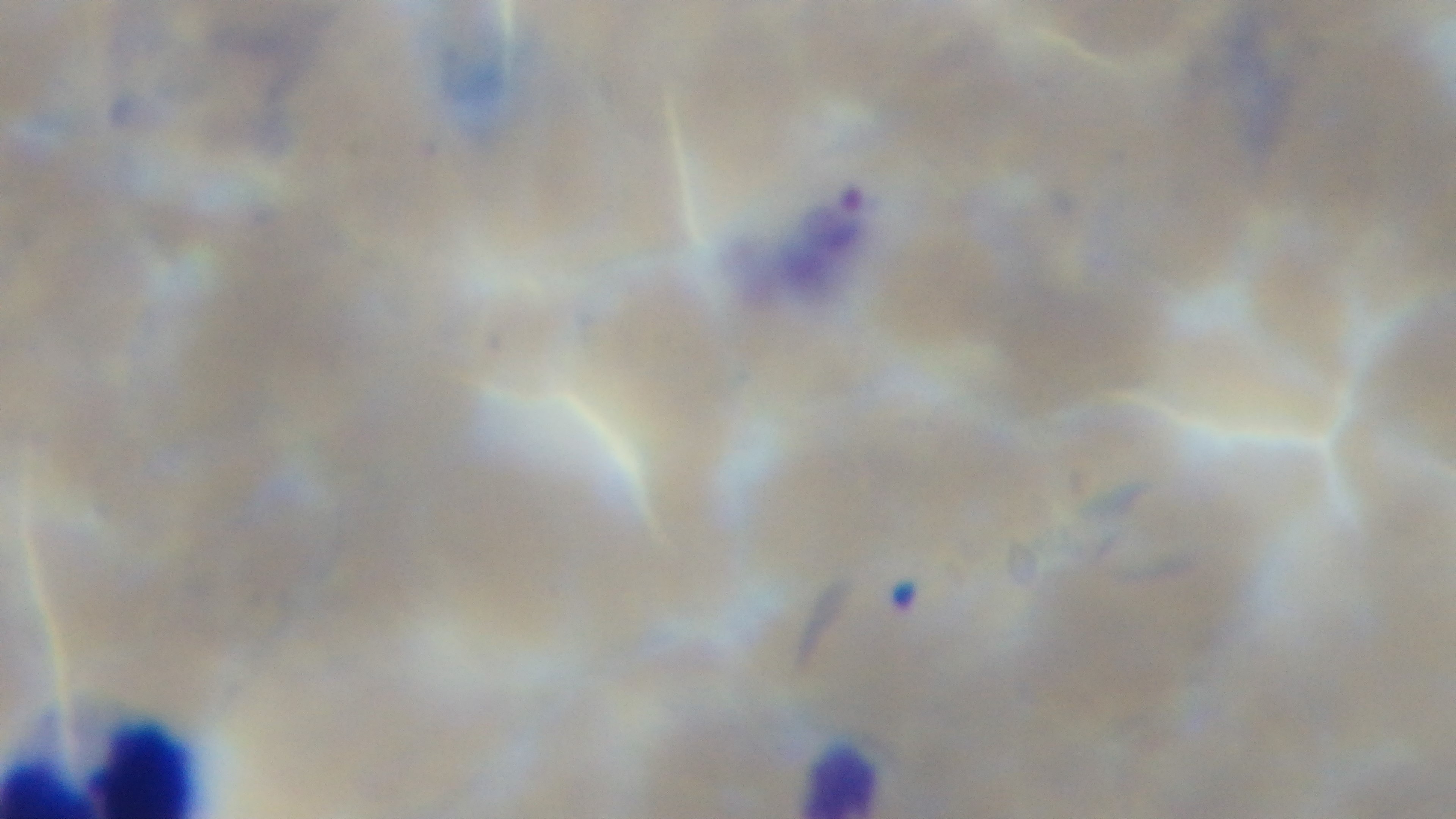
capture = mounted 4K digital camera
field of view = one from the slide
malaria status = positive
preparation = thin blood film
objective = 100x oil immersion
modality = light microscopy
stain = Giemsa